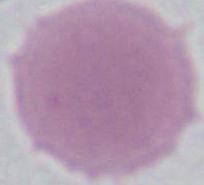
Summary:
  - Identification: erythrocyte
  - Modality: photomicrograph
  - Magnification: 1000x